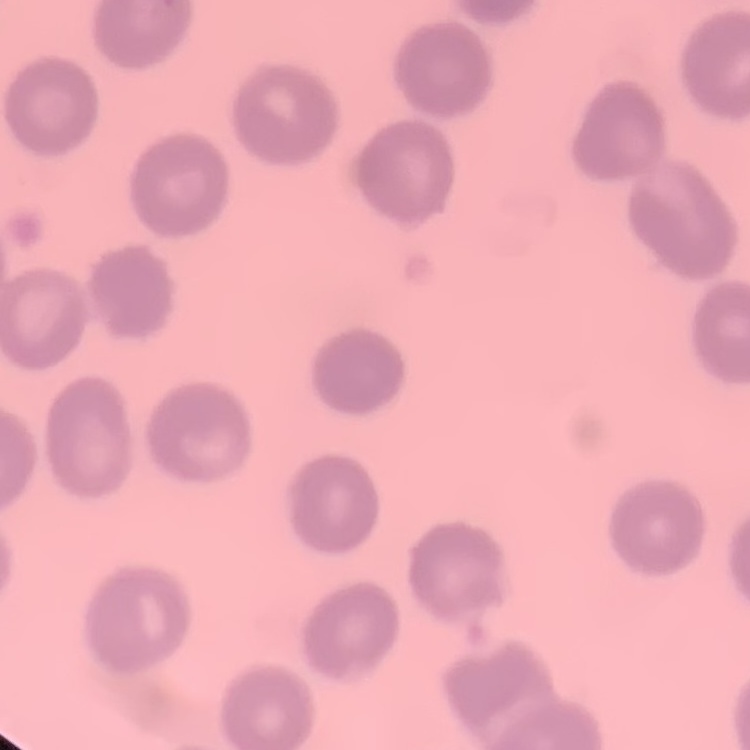

The erythrocytes exhibit no rouleaux formation. Square crop of a larger photomicrograph. Thin peripheral smear. Field's or Giemsa stain.